Name the cell type shown.
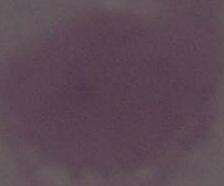
An erythrocyte.

modality = photomicrograph
magnification = 1000x